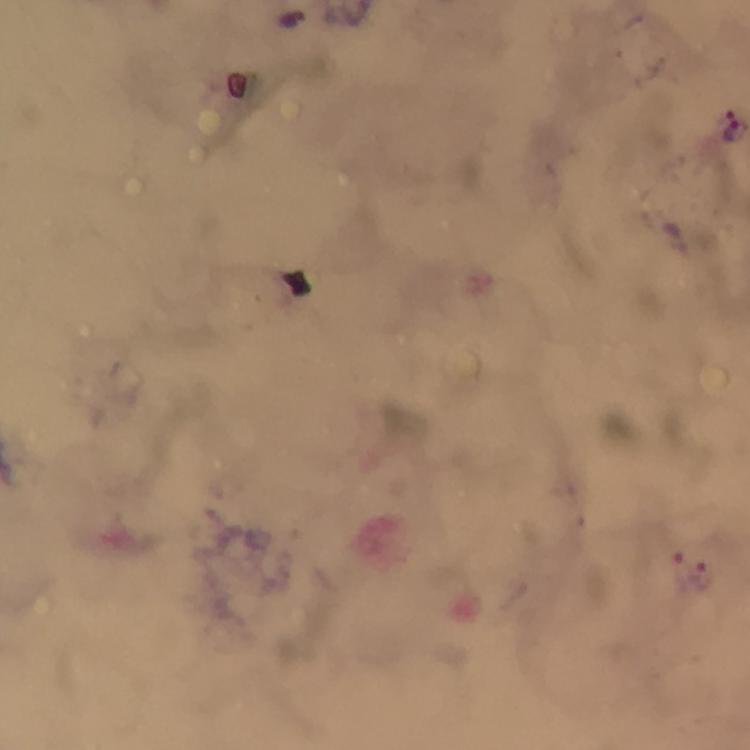 Approximate centers as [x, y] in pixels. Malaria parasite locations: [729, 125], [701, 576]. From a malaria diagnostic workup. Image is 750×750 pixels. Cropped region of a single field of view. Thick blood film. Giemsa-stained preparation. Smartphone photograph taken through a microscope. At 100x magnification. Immersion oil applied.